Classify this cell by malaria status.
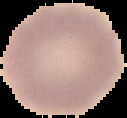

It is uninfected.

Summary:
  - Image type: cell region segmented out of the field of view; surrounding area masked to black
  - Image size: 127×118 pixels
  - Preparation: thin blood film